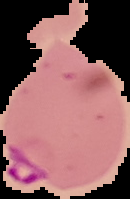
{
  "malaria_status": "parasitized",
  "image_size": "130×199 pixels",
  "image_type": "segmented cell region on a black background",
  "preparation": "thin blood film"
}